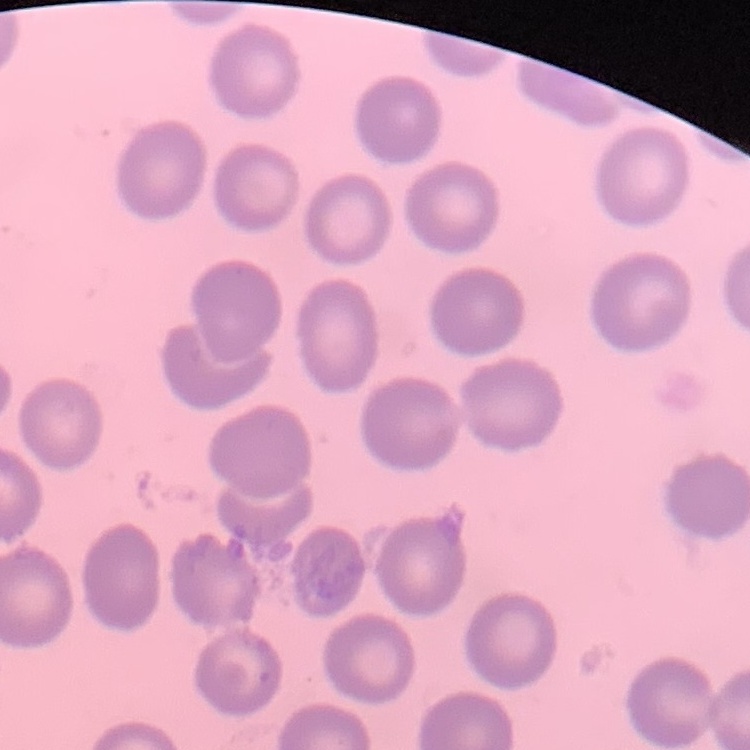
The red blood cells show no rouleaux formation. Thin blood film. One tile cut from a larger photomicrograph. Stained with either Field's or Giemsa.